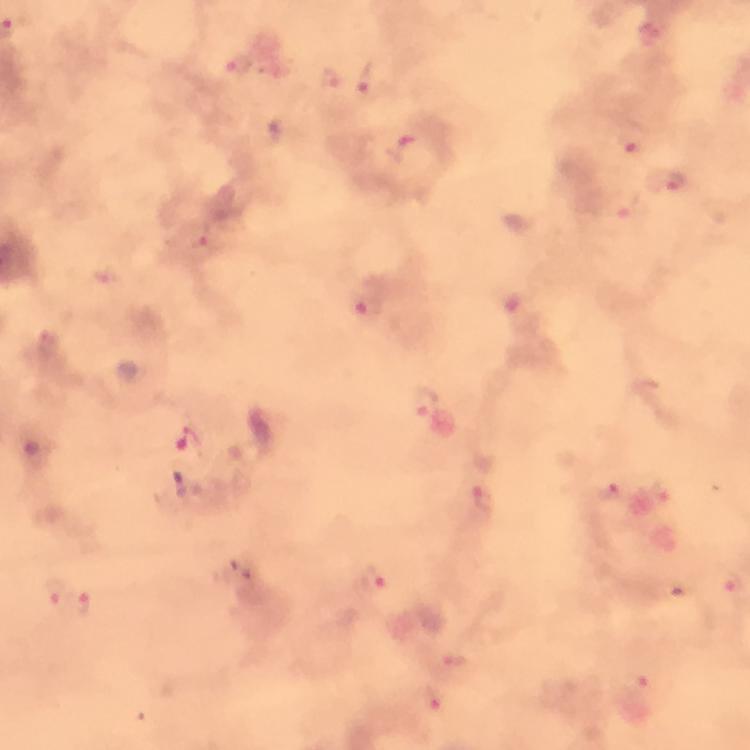

immersion_oil: used
context: from a malaria diagnostic workup
image_size: 750×750 pixels
capture: smartphone camera through the microscope
preparation: thick smear
plasmodium_parasite_locations: 'approximate centers as {x, y} in pixels: {239, 67}, {369, 78}, {330, 81}, {632, 140}, {675, 182}, {201, 238}, {369, 307}, {425, 403}, {189, 442}, {611, 493}, {486, 502}, {371, 581}, {734, 586}, {58, 594}, {82, 605}, {454, 660}, {636, 695}, {432, 702}'
magnification: 100x
stain: Giemsa
cropped_from: a single field of view